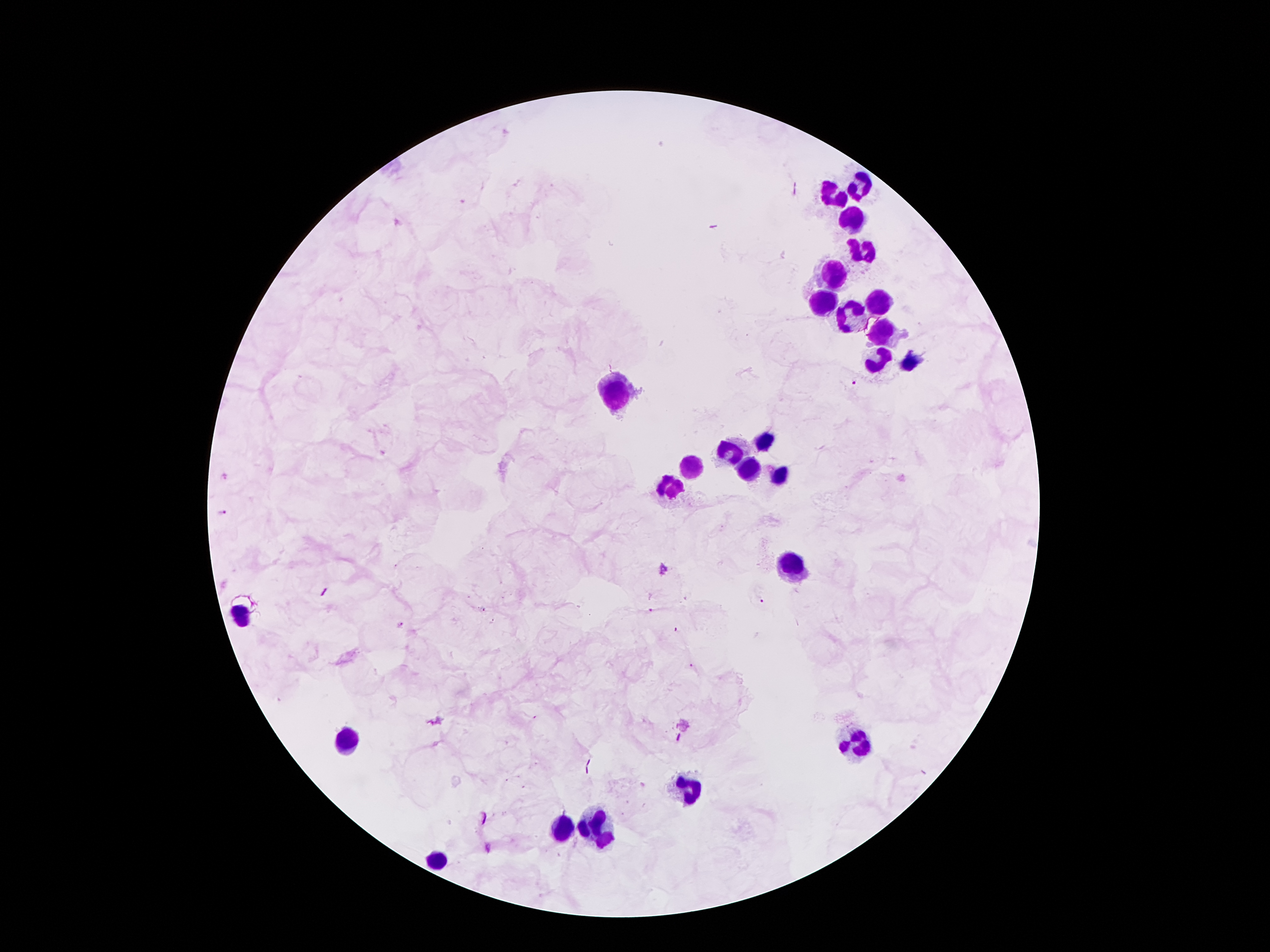

Approximate object centers, in pixels from the top-left corner. Leukocyte locations: (x=858, y=188), (x=833, y=193), (x=852, y=219), (x=862, y=250), (x=837, y=270), (x=823, y=301), (x=878, y=305), (x=852, y=318), (x=880, y=334), (x=878, y=359), (x=909, y=363), (x=618, y=393), (x=762, y=440), (x=731, y=451), (x=751, y=471), (x=688, y=473), (x=780, y=473), (x=674, y=488), (x=790, y=563), (x=240, y=613), (x=348, y=740), (x=854, y=742), (x=686, y=791), (x=594, y=830), (x=557, y=834), (x=438, y=864). Malaria parasite locations: (x=857, y=383), (x=223, y=513), (x=664, y=571), (x=761, y=601), (x=401, y=626). Patient malaria status: positive for Plasmodium falciparum. Giemsa stain. Single field of view. 100x magnification. Thick blood film. Image is 1270×952 pixels. Photographed through the microscope eyepiece with a smartphone camera.